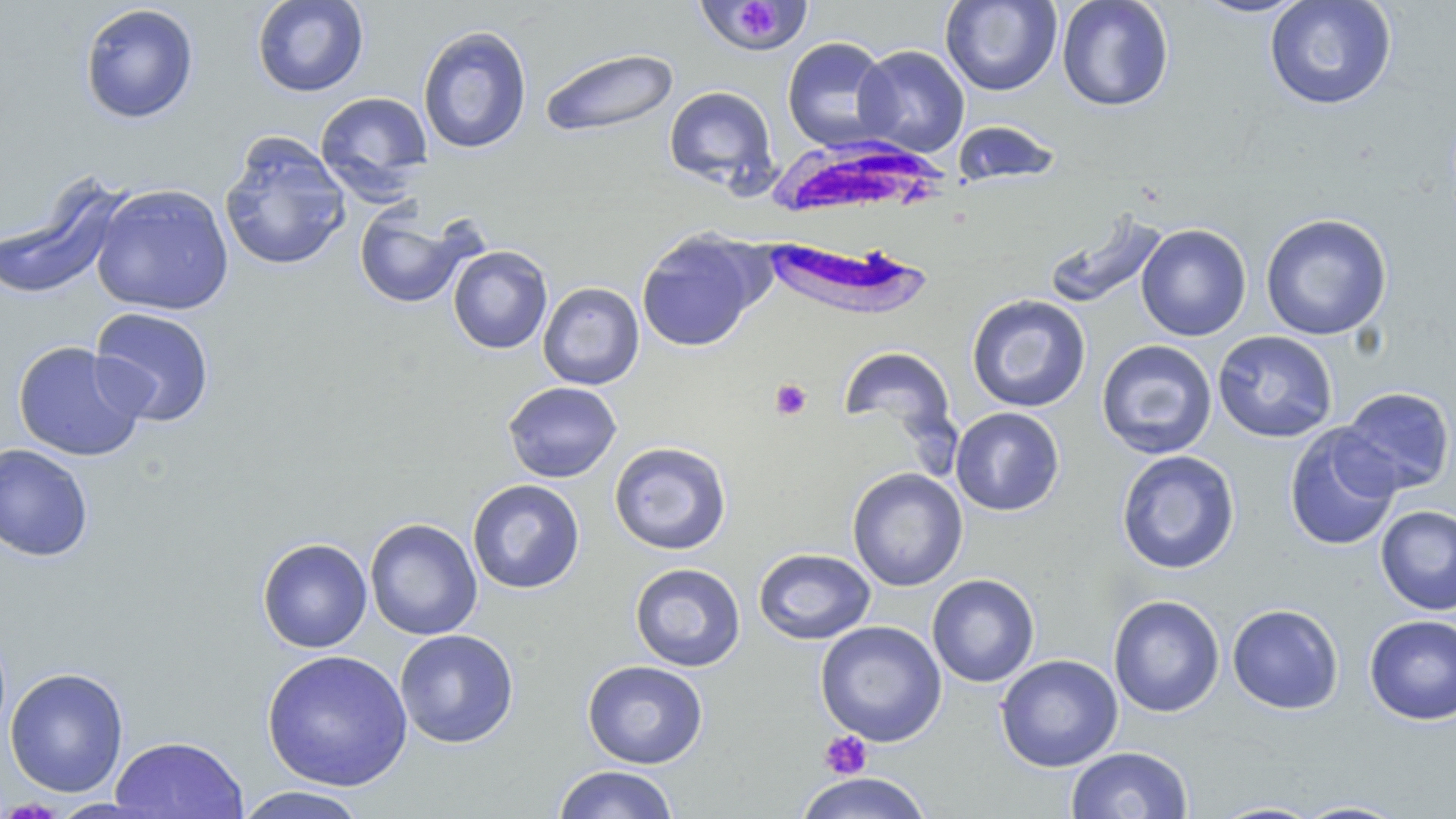

slide_level_diagnosis: Plasmodium falciparum
platelet_locations: 'approximate bounding boxes as named x1/y1/x2/y2 corners in pixels: (x1=738, y1=1, x2=777, y2=40), (x1=770, y1=378, x2=812, y2=420), (x1=819, y1=731, x2=872, y2=779)'
magnification: 1000x
preparation: thin blood smear
stain: May-Grünwald-Giemsa
image_size: 1456×819 pixels
white_blood_cell_locations: 'approximate bounding boxes as named x1/y1/x2/y2 corners in pixels: (x1=771, y1=144, x2=971, y2=317)'
modality: optical microscopy
uninfected_red_blood_cell_locations: 'approximate bounding boxes as named x1/y1/x2/y2 corners in pixels: (x1=252, y1=0, x2=369, y2=97), (x1=699, y1=0, x2=820, y2=53), (x1=940, y1=0, x2=1062, y2=96), (x1=1056, y1=0, x2=1175, y2=112), (x1=1189, y1=0, x2=1314, y2=19), (x1=1264, y1=1, x2=1397, y2=111), (x1=79, y1=3, x2=199, y2=124), (x1=417, y1=25, x2=532, y2=154), (x1=782, y1=36, x2=896, y2=152), (x1=853, y1=45, x2=970, y2=157), (x1=539, y1=47, x2=679, y2=139), (x1=663, y1=85, x2=777, y2=190), (x1=315, y1=91, x2=434, y2=198), (x1=950, y1=120, x2=1063, y2=187), (x1=219, y1=132, x2=351, y2=272), (x1=0, y1=181, x2=124, y2=301), (x1=90, y1=182, x2=235, y2=316), (x1=354, y1=205, x2=474, y2=309), (x1=1043, y1=209, x2=1169, y2=310), (x1=1260, y1=213, x2=1392, y2=341), (x1=1135, y1=223, x2=1252, y2=341), (x1=636, y1=229, x2=764, y2=352), (x1=447, y1=245, x2=553, y2=354), (x1=538, y1=282, x2=644, y2=390), (x1=966, y1=294, x2=1091, y2=413), (x1=89, y1=306, x2=216, y2=428), (x1=1212, y1=330, x2=1338, y2=443), (x1=1096, y1=339, x2=1217, y2=459), (x1=12, y1=340, x2=148, y2=462), (x1=838, y1=346, x2=958, y2=445), (x1=502, y1=381, x2=621, y2=483), (x1=1337, y1=386, x2=1455, y2=496), (x1=950, y1=407, x2=1065, y2=516), (x1=1284, y1=424, x2=1402, y2=552), (x1=609, y1=441, x2=732, y2=555), (x1=0, y1=443, x2=94, y2=561), (x1=1116, y1=450, x2=1240, y2=574), (x1=847, y1=468, x2=968, y2=591), (x1=467, y1=479, x2=585, y2=594), (x1=1375, y1=504, x2=1456, y2=615), (x1=365, y1=518, x2=482, y2=640), (x1=257, y1=538, x2=372, y2=653), (x1=753, y1=548, x2=876, y2=645), (x1=629, y1=563, x2=746, y2=672), (x1=926, y1=573, x2=1040, y2=687), (x1=1108, y1=594, x2=1225, y2=718), (x1=1227, y1=603, x2=1344, y2=715), (x1=1364, y1=614, x2=1456, y2=725), (x1=815, y1=620, x2=946, y2=747), (x1=394, y1=629, x2=519, y2=749), (x1=261, y1=649, x2=413, y2=791), (x1=995, y1=653, x2=1123, y2=772), (x1=582, y1=660, x2=709, y2=769), (x1=5, y1=667, x2=129, y2=797), (x1=110, y1=735, x2=248, y2=819), (x1=1066, y1=746, x2=1194, y2=818), (x1=552, y1=765, x2=680, y2=818), (x1=794, y1=773, x2=935, y2=819), (x1=233, y1=786, x2=370, y2=819), (x1=1292, y1=799, x2=1412, y2=818), (x1=1206, y1=800, x2=1326, y2=818)'
field_of_view: single